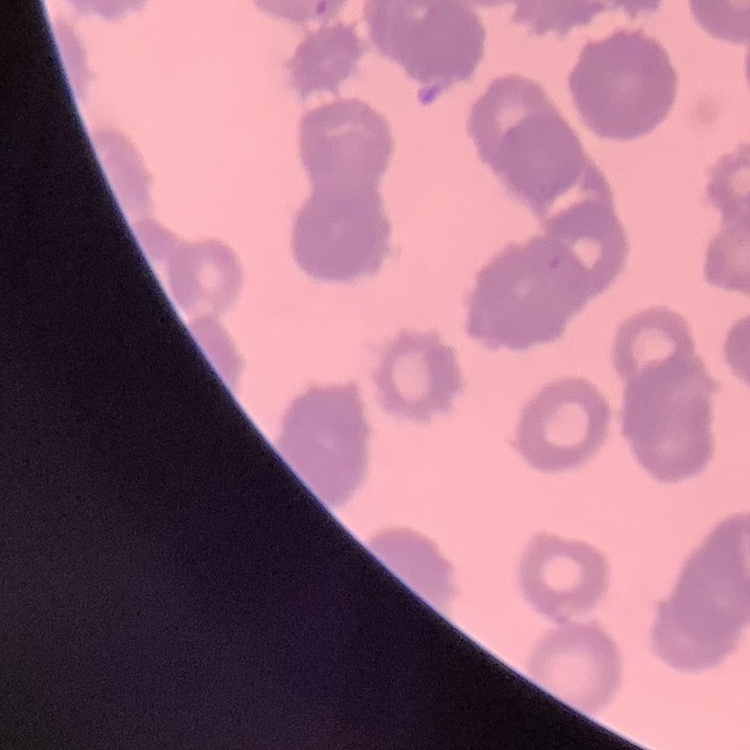

erythrocyte morphology = rouleaux formation
stain = Field's or Giemsa
preparation = thin blood film
image type = one tile cut from a larger photomicrograph